Assess this cell for malaria.
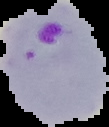
It is parasitized.

{
  "image_size": "109×127 pixels",
  "preparation": "thin blood film",
  "image_type": "cell region segmented out of the field of view; surrounding area masked to black"
}